State which cell type is depicted.
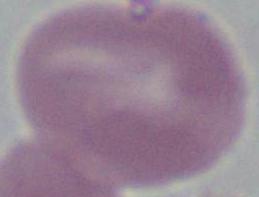
An erythrocyte.

Summary:
  - Modality: micrograph
  - Magnification: 1000x